Outline every malaria parasite, every leukocyte, and every artifact (stain precipitate or debris).
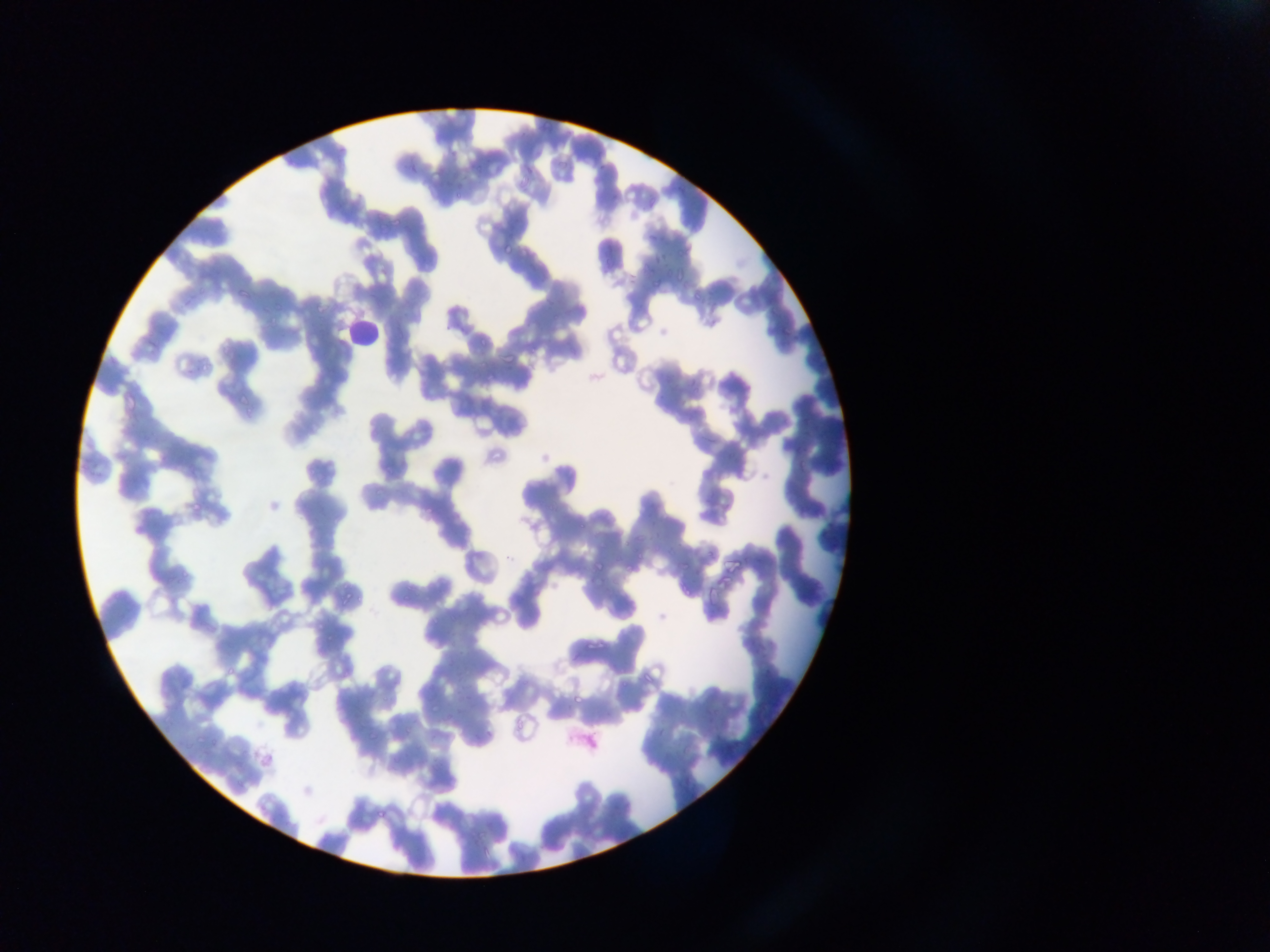

Approximate bounding boxes as (left, top, right, bottom) in pixels.
Malaria parasites: (536, 113, 553, 133), (520, 159, 545, 189), (556, 161, 569, 173), (452, 192, 461, 200), (375, 206, 386, 224), (389, 217, 402, 230), (501, 227, 523, 259), (671, 264, 685, 279), (651, 274, 657, 286), (236, 286, 258, 301), (690, 286, 704, 306), (310, 298, 330, 320), (273, 300, 285, 315), (267, 313, 280, 326), (477, 323, 492, 346), (498, 352, 516, 361), (197, 353, 214, 372), (238, 388, 254, 408), (190, 499, 205, 514), (575, 517, 586, 532), (636, 546, 646, 563), (596, 557, 614, 572), (624, 559, 637, 584), (723, 560, 747, 575), (678, 561, 688, 573), (678, 575, 694, 600), (704, 576, 721, 605), (345, 582, 355, 591), (339, 592, 354, 605), (359, 597, 367, 608), (584, 630, 604, 652), (322, 634, 333, 648), (224, 664, 239, 680), (641, 667, 652, 682), (571, 688, 588, 710), (425, 700, 438, 715), (512, 716, 529, 730), (365, 728, 380, 746), (193, 734, 202, 744), (212, 735, 220, 748), (374, 800, 389, 820).
Leukocytes: (343, 308, 378, 347).

Summary:
  - Preparation: thin blood smear
  - Image size: 1270×952 pixels
  - Country: Ghana
  - Field of view: single
  - Capture: mobile-phone photograph through a microscope